Assess this cell for malaria.
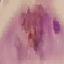
Parasitized.

image_type: cell patch, automatically extracted from a larger field of view and resized to 64 × 64 pixels
preparation: thin blood film
stain: Giemsa
capture: smartphone through the microscope eyepiece